Describe the morphology of the erythrocytes.
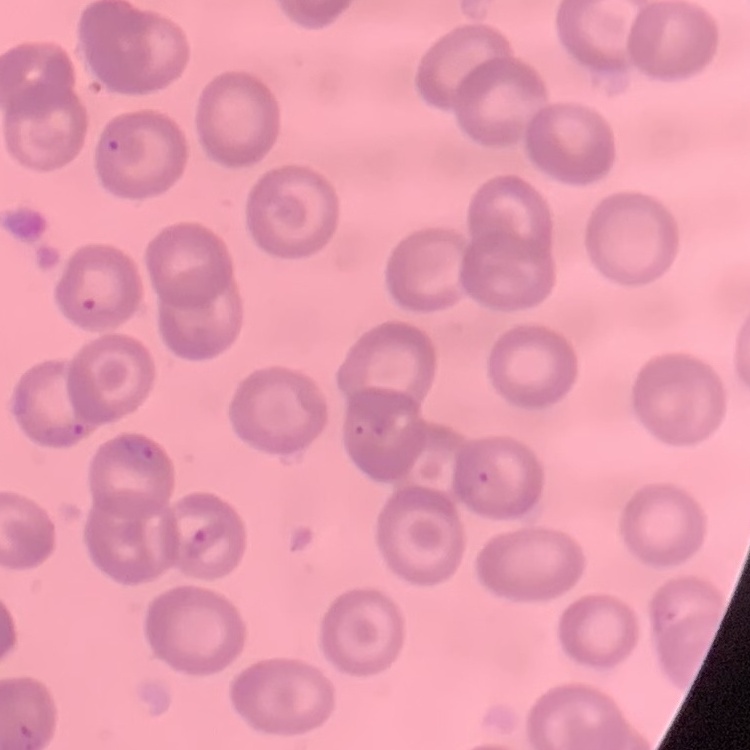

They show no rouleaux formation.

Thin blood smear. Square crop of a larger photomicrograph. Stained with either Field's or Giemsa.